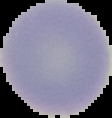
Summary:
  - Malaria status: uninfected
  - Image type: cell region segmented out of the field of view; surrounding area masked to black
  - Preparation: thin blood film
  - Image size: 112×118 pixels